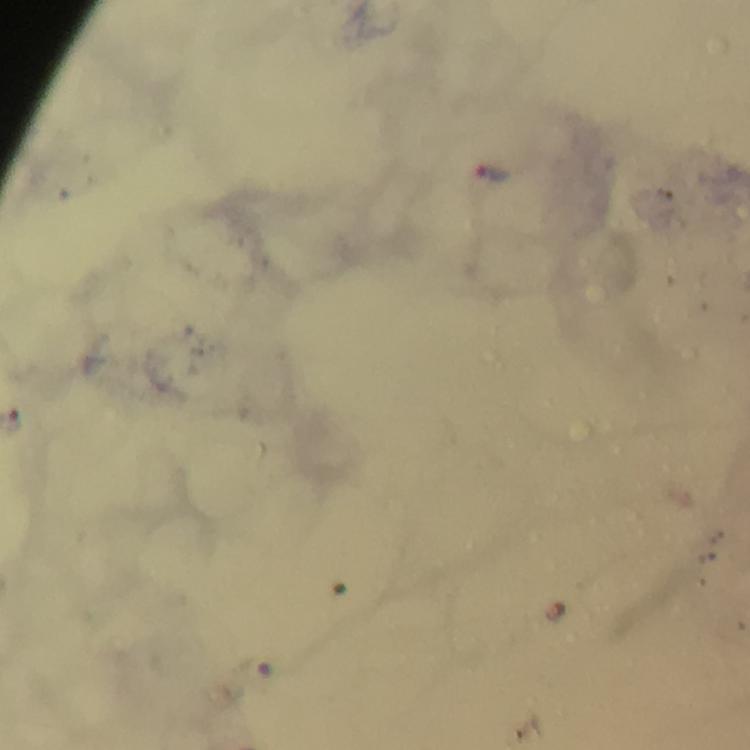
Approximate centers as {x, y} in pixels. Malaria parasite locations: {495, 172}. A crop from one field of view. Smartphone photograph taken through a microscope. Image is 750×750 pixels. Immersion oil was used. Giemsa-stained preparation. From a malaria diagnostic workup. Thick smear. 100x magnification.